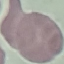

Summary:
  - Result: no malaria parasites detected
  - Stain: Giemsa
  - Image type: cell patch, automatically extracted from a larger field of view and resized to 64 × 64 pixels
  - Capture: smartphone camera at the microscope eyepiece
  - Preparation: thin smear